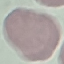
result = no malaria parasites seen
capture = smartphone through the microscope eyepiece
stain = Giemsa
preparation = thin blood film
image type = cell patch, automatically extracted from a larger field of view and resized to 64 × 64 pixels